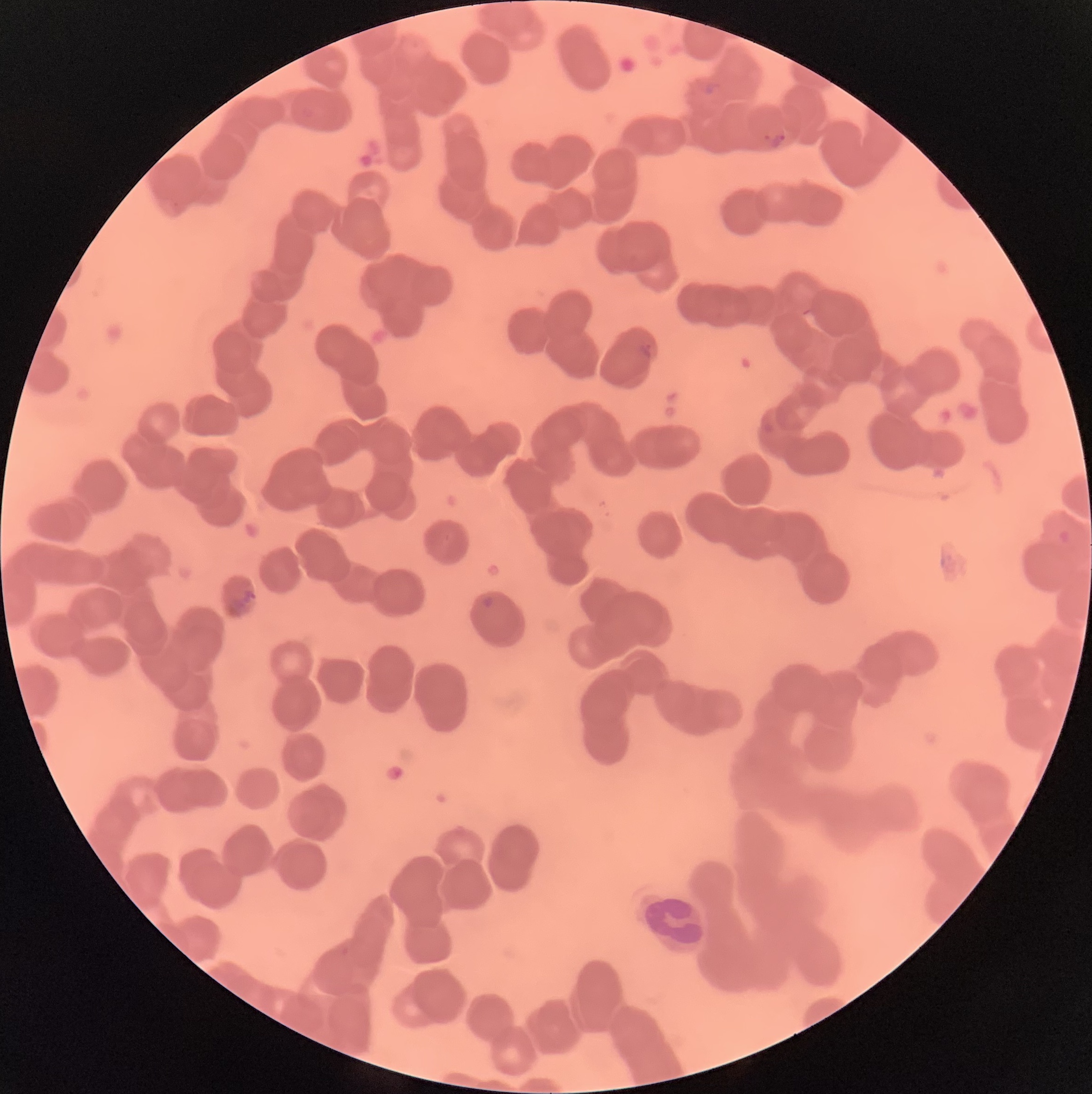

Approximate bounding boxes as [x1, y1, x2, y2] in pixels. Plasmodium parasite locations: [700, 81, 720, 95], [762, 130, 786, 148], [636, 340, 655, 359], [227, 589, 257, 615], [480, 596, 495, 608]. White blood cell locations: [640, 895, 710, 955]. Thin blood film. Image is 1092×1094 pixels. Light microscopy. The red blood cells show rouleaux formation.